Classify this cell by malaria status.
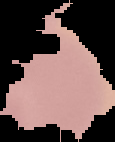

Uninfected.

Summary:
  - Image size: 115×142 pixels
  - Preparation: thin blood film
  - Image type: cell region segmented out of the field of view; surrounding area masked to black